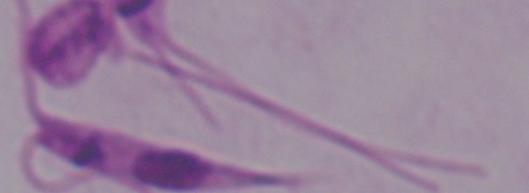 Photomicrograph. 1000x magnification. A Leishmania parasite is seen.